Locate and identify every blood parasite.
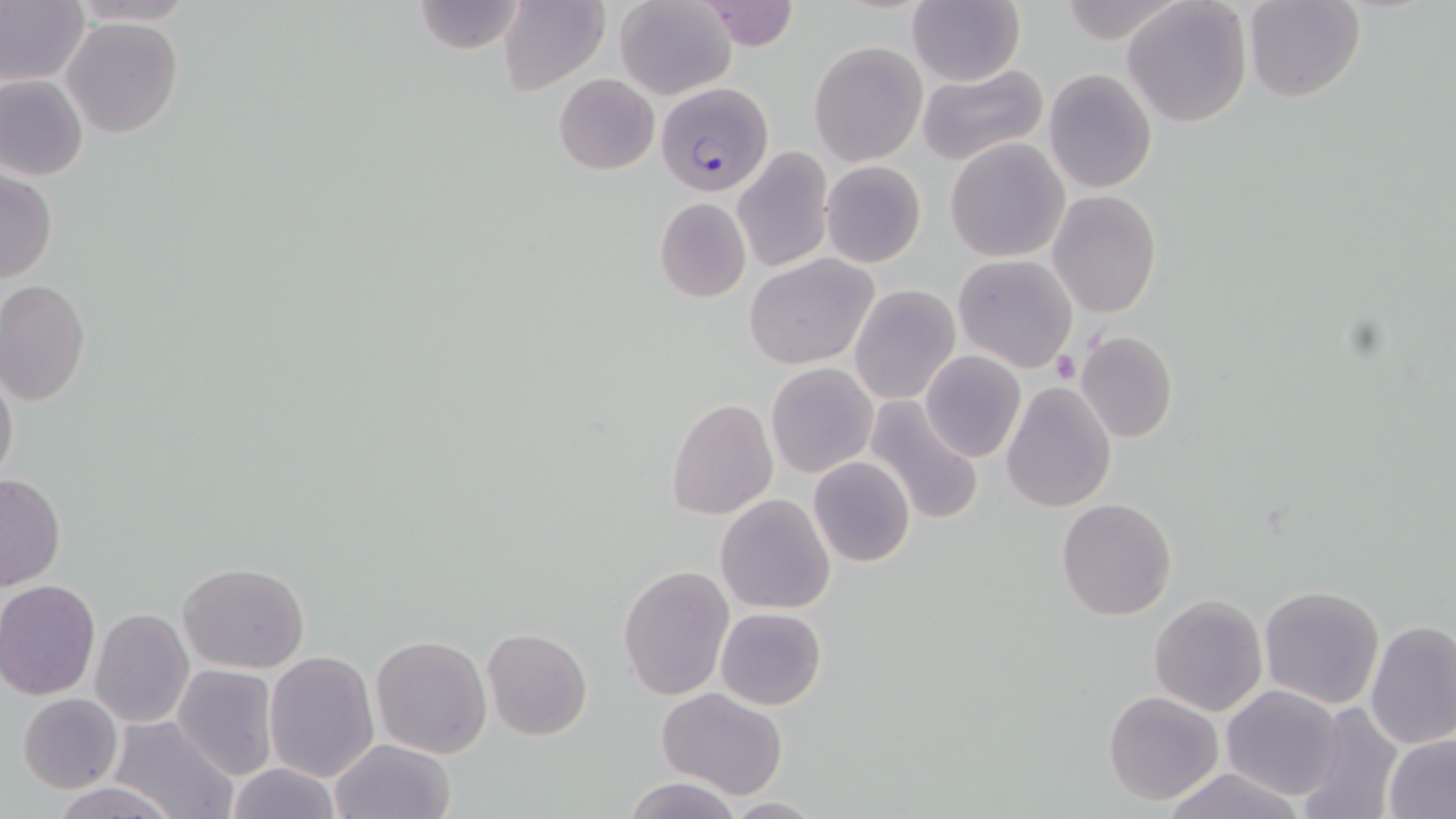
Approximate bounding boxes as [x1, y1, x2, y2] in pixels.
Plasmodium falciparum-infected red blood cells: [656, 83, 774, 196].
No Plasmodium ovale, Plasmodium malariae, Plasmodium vivax, Babesia divergens, or Trypanosoma brucei observed.

Uninfected red blood cell locations: [0, 0, 89, 87], [64, 0, 202, 26], [499, 0, 610, 95], [616, 0, 737, 100], [1122, 0, 1254, 127], [414, 1, 524, 54], [696, 1, 798, 51], [1055, 1, 1186, 44], [1242, 1, 1365, 103], [906, 2, 1025, 86], [61, 18, 183, 137], [809, 41, 927, 166], [916, 65, 1048, 167], [1044, 70, 1157, 193], [0, 74, 89, 181], [554, 74, 659, 174], [945, 140, 1069, 262], [731, 147, 834, 274], [821, 160, 927, 268], [0, 169, 58, 283], [1048, 190, 1161, 318], [654, 197, 752, 302], [745, 254, 878, 370], [953, 254, 1078, 373], [0, 279, 91, 404], [849, 285, 960, 404], [1074, 330, 1179, 444], [919, 350, 1026, 463], [1, 362, 19, 489], [766, 363, 879, 478], [1002, 382, 1116, 513], [864, 396, 985, 526], [667, 399, 778, 519], [808, 457, 916, 567], [0, 473, 67, 592], [715, 494, 836, 613], [1057, 498, 1177, 621], [178, 562, 309, 674], [618, 565, 734, 700], [0, 580, 101, 699], [1258, 583, 1385, 710], [1149, 596, 1268, 716], [716, 607, 827, 710], [90, 609, 195, 728], [1365, 620, 1456, 752], [482, 627, 593, 741], [371, 634, 492, 757], [264, 650, 380, 781], [172, 665, 278, 780], [1220, 684, 1345, 801], [656, 687, 789, 799], [1103, 691, 1224, 805], [18, 692, 124, 793], [1297, 701, 1403, 819], [108, 714, 237, 819], [1383, 732, 1455, 818], [329, 739, 456, 819], [225, 762, 342, 819], [1158, 767, 1307, 819], [623, 776, 742, 819], [54, 781, 176, 819], [719, 796, 827, 817]. Platelet locations: [1052, 350, 1081, 383]. Slide-level diagnosis: Plasmodium falciparum. May-Grünwald-Giemsa-stained preparation. Light microscopy. Image is 1456×819 pixels. One field of a larger specimen. 1000x magnification. Thin blood smear.